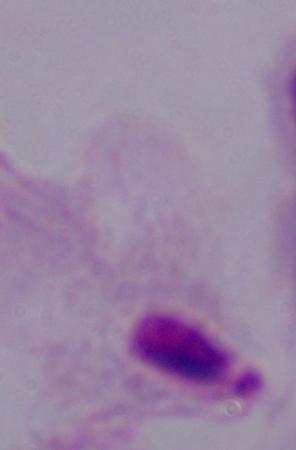 A trichomonad is shown. Photomicrograph. Captured at 1000x magnification.